Comment on the morphology of the red blood cells.
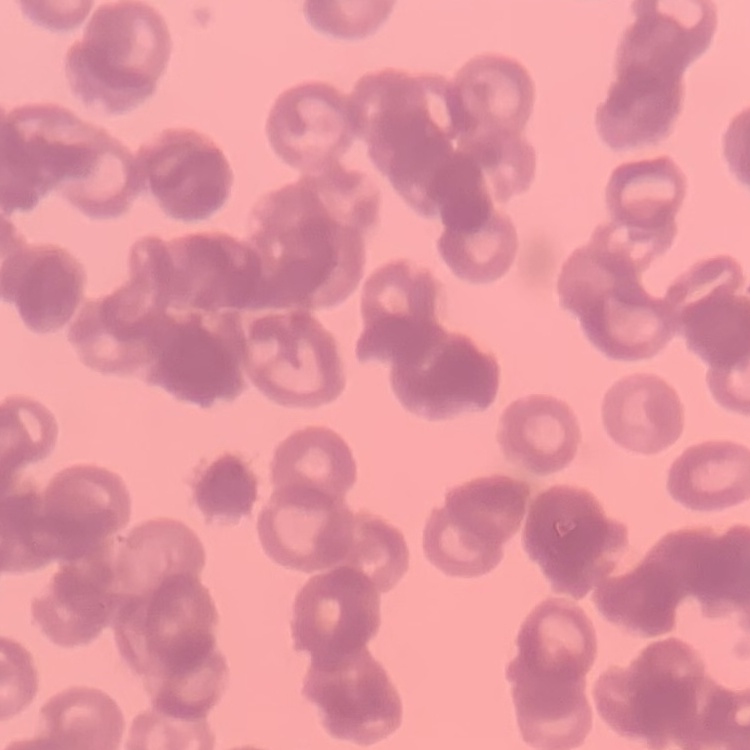
Rouleaux formation.

stain: Field's or Giemsa
preparation: thin peripheral smear
image_type: one tile cut from a larger photomicrograph